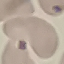

{
  "result": "no malaria parasites detected",
  "preparation": "thin blood film",
  "image_type": "automatically extracted cell patch, resized to 64 × 64 pixels",
  "capture": "smartphone through the microscope eyepiece",
  "stain": "Giemsa"
}